Assess this cell for malaria.
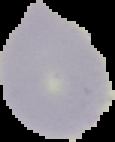

Uninfected.

image_type: cell region segmented out of the field of view; surrounding area masked to black
preparation: thin blood film
image_size: 115×142 pixels